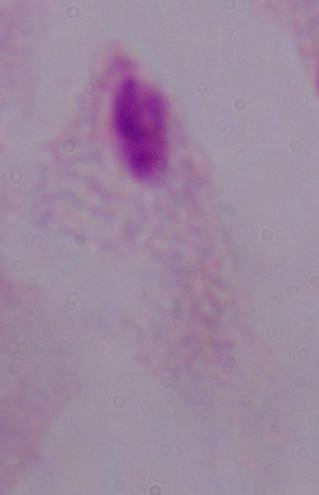

magnification = 1000x
modality = micrograph
identification = trichomonad